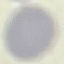

Malaria status: uninfected. Thin smear of blood. Automatically extracted cell patch, resized to 64 × 64 pixels. Acquired by smartphone through the microscope eyepiece. Giemsa stain.